Give the location of every white blood cell.
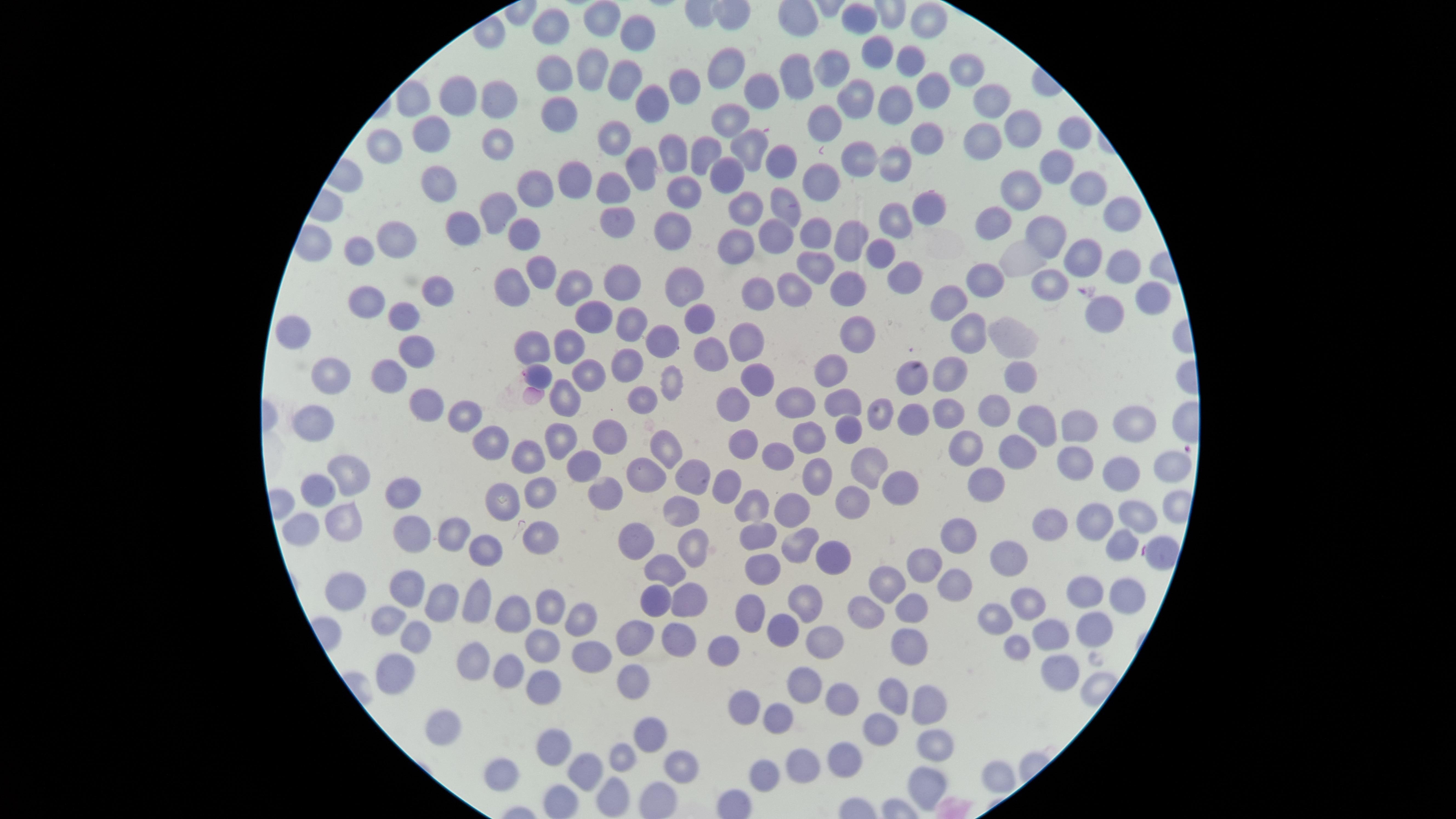

No white blood cells identified.

Approximate marker points, in pixels from the top-left corner.
Summary:
  - Uninfected red blood cells: (x=608, y=17), (x=864, y=22), (x=925, y=22), (x=550, y=30), (x=639, y=33), (x=872, y=51), (x=903, y=58), (x=596, y=62), (x=973, y=67), (x=736, y=70), (x=832, y=71), (x=551, y=73), (x=791, y=78), (x=632, y=79), (x=922, y=85), (x=689, y=86), (x=760, y=87), (x=461, y=93), (x=856, y=95), (x=422, y=97), (x=1001, y=97), (x=652, y=98), (x=497, y=100), (x=894, y=100), (x=559, y=111), (x=734, y=115), (x=826, y=123), (x=1022, y=129), (x=432, y=132), (x=618, y=132), (x=1074, y=133), (x=926, y=134), (x=979, y=140), (x=500, y=142), (x=749, y=142), (x=699, y=148), (x=379, y=149), (x=670, y=151), (x=778, y=155), (x=856, y=157), (x=893, y=158), (x=636, y=164), (x=1047, y=165), (x=727, y=173), (x=434, y=176), (x=567, y=180), (x=823, y=182), (x=530, y=187), (x=615, y=190), (x=1092, y=191), (x=1019, y=193), (x=684, y=198), (x=784, y=206), (x=922, y=207), (x=745, y=208), (x=497, y=210), (x=1116, y=214), (x=993, y=219), (x=615, y=221), (x=892, y=221), (x=467, y=222), (x=668, y=227), (x=775, y=231), (x=814, y=231), (x=857, y=232), (x=526, y=233), (x=396, y=234), (x=1051, y=234), (x=744, y=243), (x=359, y=250), (x=1026, y=256), (x=879, y=257), (x=1081, y=260), (x=1123, y=263), (x=816, y=265), (x=542, y=270), (x=898, y=274), (x=988, y=274), (x=690, y=276), (x=621, y=277), (x=1050, y=280), (x=798, y=285), (x=516, y=286), (x=758, y=288), (x=849, y=290), (x=1145, y=291), (x=572, y=292), (x=370, y=296), (x=438, y=297), (x=951, y=300), (x=405, y=304), (x=1102, y=313), (x=691, y=314), (x=588, y=317), (x=630, y=320), (x=289, y=327), (x=852, y=328), (x=967, y=331), (x=1015, y=332), (x=662, y=336), (x=572, y=339), (x=751, y=339), (x=418, y=342), (x=532, y=343), (x=709, y=351), (x=631, y=364), (x=835, y=368), (x=948, y=370), (x=389, y=371), (x=539, y=372), (x=754, y=373), (x=908, y=373), (x=1006, y=374), (x=585, y=375), (x=334, y=376), (x=673, y=376), (x=568, y=395), (x=791, y=397), (x=736, y=399), (x=643, y=400), (x=841, y=402), (x=990, y=402), (x=426, y=403), (x=916, y=407), (x=945, y=410), (x=881, y=413), (x=466, y=417), (x=1127, y=420), (x=317, y=423), (x=1044, y=423), (x=852, y=428), (x=1079, y=428), (x=609, y=434), (x=563, y=435), (x=743, y=437), (x=495, y=440), (x=810, y=441), (x=666, y=443), (x=978, y=449), (x=531, y=450), (x=1020, y=451), (x=778, y=454), (x=580, y=462), (x=1081, y=462), (x=862, y=464), (x=345, y=468), (x=692, y=471), (x=1166, y=472), (x=1120, y=475), (x=648, y=476), (x=981, y=477), (x=824, y=479), (x=722, y=483), (x=321, y=485), (x=894, y=487), (x=540, y=488), (x=401, y=490), (x=604, y=490), (x=503, y=498), (x=849, y=501), (x=752, y=503), (x=681, y=507), (x=789, y=509), (x=1140, y=513), (x=1094, y=521), (x=348, y=522), (x=1054, y=524), (x=309, y=526), (x=450, y=530), (x=416, y=531), (x=754, y=532), (x=538, y=534), (x=963, y=538), (x=633, y=544), (x=483, y=546), (x=793, y=546), (x=689, y=548), (x=1114, y=549), (x=823, y=555), (x=1162, y=555), (x=1009, y=556), (x=925, y=561), (x=762, y=566), (x=662, y=570), (x=889, y=578), (x=953, y=583), (x=405, y=586), (x=1127, y=589), (x=352, y=591), (x=1082, y=593), (x=806, y=596), (x=656, y=598), (x=684, y=598), (x=479, y=600), (x=438, y=604), (x=1030, y=604), (x=909, y=605), (x=540, y=606), (x=751, y=607), (x=868, y=608), (x=507, y=613), (x=581, y=613), (x=1001, y=613), (x=387, y=619), (x=1090, y=621), (x=780, y=625), (x=1046, y=631), (x=418, y=633), (x=675, y=634), (x=629, y=635), (x=547, y=641), (x=815, y=641), (x=900, y=641), (x=1016, y=646), (x=728, y=649), (x=595, y=650), (x=475, y=657), (x=1049, y=669), (x=392, y=671), (x=510, y=671), (x=540, y=682), (x=805, y=682), (x=627, y=683), (x=890, y=693), (x=930, y=698), (x=741, y=702), (x=847, y=702), (x=780, y=717), (x=444, y=719), (x=877, y=726), (x=647, y=734), (x=928, y=743), (x=555, y=744), (x=853, y=751), (x=621, y=753), (x=674, y=757), (x=497, y=763), (x=998, y=772), (x=803, y=774), (x=585, y=776), (x=764, y=776), (x=923, y=778), (x=613, y=799), (x=561, y=800), (x=655, y=800)
  - Stain: Giemsa
  - Presence: no malaria parasites detected
  - Preparation: thin blood film
  - Field of view: single
  - Visible region: circular
  - Capture: smartphone photograph through the microscope eyepiece
  - Image size: 1456×819 pixels